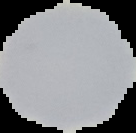

Summary:
  - Preparation: thin blood film
  - Malaria status: uninfected
  - Image type: segmented cell region on a black background
  - Image size: 136×133 pixels